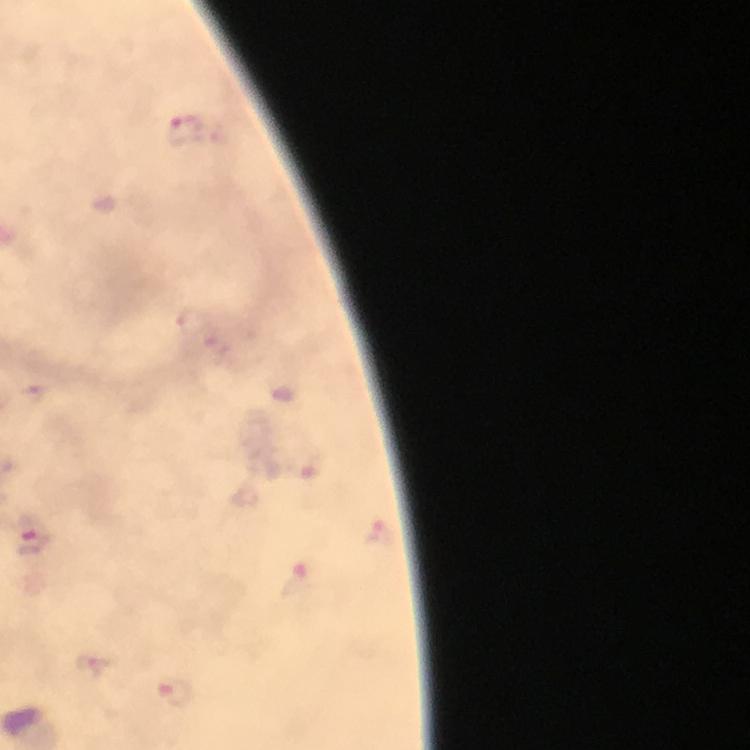

Approximate centers as (x, y) in pixels.
Summary:
  - Malaria parasite locations: (186, 130), (192, 323), (36, 394), (381, 531), (35, 537), (303, 580), (176, 693)
  - Cropped from: a single field of view
  - Image size: 750×750 pixels
  - Stain: Giemsa
  - Magnification: 100x
  - Immersion oil: applied
  - Preparation: thick blood film
  - Context: from a diagnostic examination for malaria
  - Capture: smartphone camera through the microscope